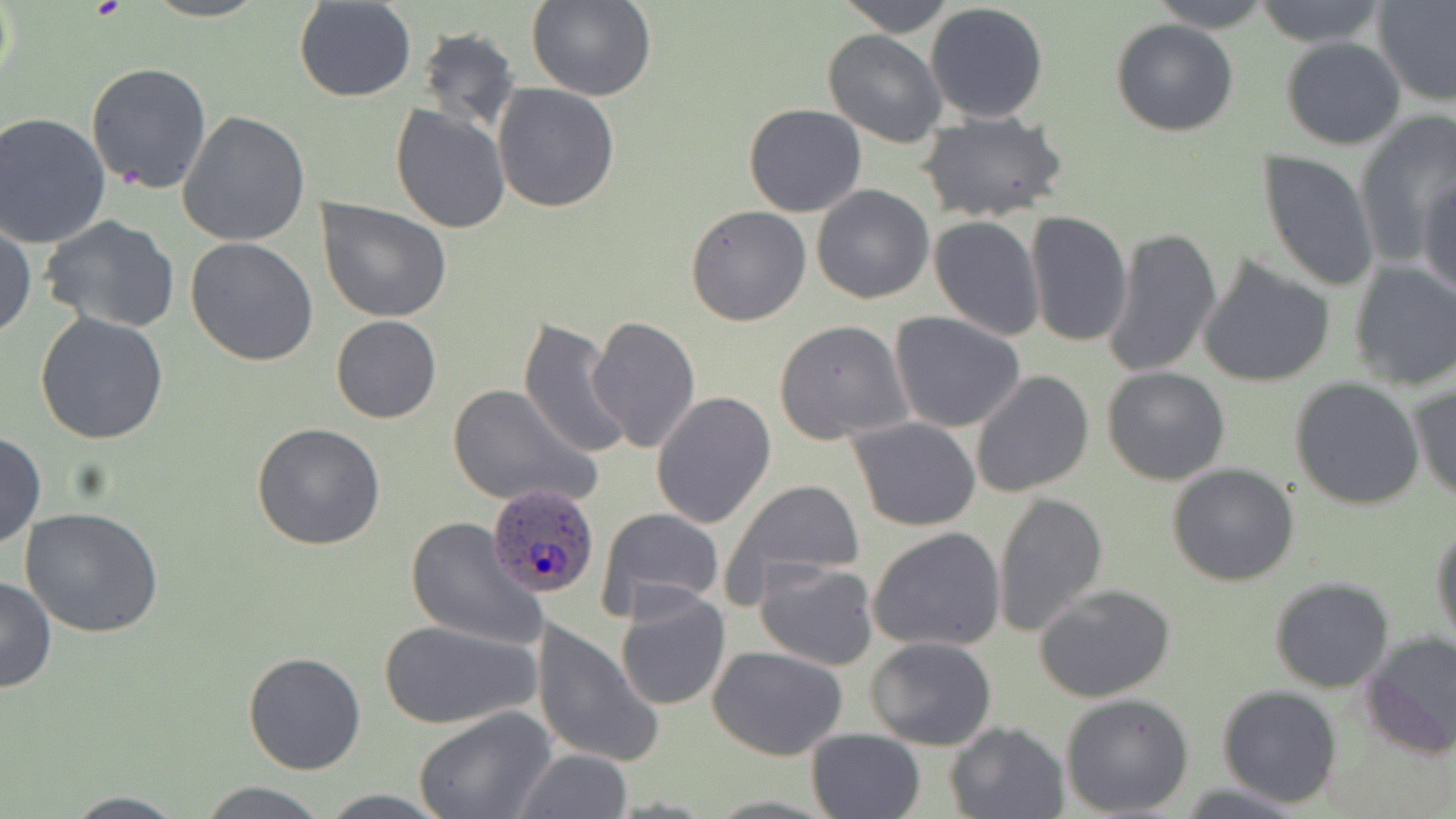 Approximate bounding boxes as [x1, y1, x2, y2] in pixels. Platelet locations: [88, 0, 129, 23]. Plasmodium ovale-infected red blood cell locations: [478, 486, 597, 604]. Uninfected red blood cell locations: [836, 0, 956, 36], [1148, 0, 1277, 32], [1251, 0, 1389, 48], [293, 1, 417, 102], [526, 1, 658, 103], [1373, 1, 1456, 105], [925, 3, 1050, 124], [1110, 18, 1239, 136], [415, 28, 522, 133], [822, 29, 947, 147], [1280, 37, 1406, 151], [85, 62, 212, 195], [492, 83, 620, 213], [743, 103, 867, 217], [389, 105, 510, 232], [178, 111, 311, 247], [919, 112, 1068, 224], [1353, 112, 1456, 265], [1, 113, 114, 250], [760, 115, 904, 263], [1258, 150, 1379, 292], [1420, 173, 1456, 301], [811, 184, 935, 304], [318, 198, 451, 323], [685, 204, 811, 325], [1024, 211, 1131, 348], [930, 215, 1045, 340], [40, 216, 182, 334], [0, 220, 36, 341], [1101, 223, 1224, 381], [186, 238, 318, 367], [1198, 256, 1336, 388], [1347, 261, 1456, 392], [889, 311, 1026, 432], [34, 312, 169, 445], [330, 315, 441, 424], [587, 316, 701, 454], [516, 320, 630, 460], [773, 320, 915, 444], [1101, 366, 1231, 485], [970, 369, 1094, 498], [1291, 377, 1425, 509], [1408, 380, 1456, 504], [447, 382, 598, 509], [651, 392, 776, 529], [847, 417, 982, 532], [252, 423, 385, 551], [0, 431, 45, 549], [1167, 463, 1300, 587], [721, 478, 866, 600], [992, 491, 1107, 639], [19, 506, 164, 638], [594, 507, 727, 623], [405, 516, 544, 651], [1431, 518, 1455, 654], [866, 526, 1007, 653], [753, 558, 878, 672], [0, 576, 57, 693], [1268, 577, 1395, 693], [1034, 583, 1176, 702], [614, 588, 732, 710], [377, 618, 541, 731], [529, 619, 662, 769], [1361, 630, 1456, 758], [866, 636, 998, 750], [708, 645, 848, 759], [243, 650, 366, 775], [1216, 685, 1343, 808], [1059, 693, 1195, 817], [414, 708, 559, 819], [944, 721, 1069, 818], [805, 728, 926, 818], [513, 749, 631, 818], [195, 780, 334, 818], [314, 789, 455, 819], [61, 792, 191, 819]. Slide-level diagnosis: Plasmodium ovale. One field of a larger specimen. 1000x magnification. May-Grünwald-Giemsa stain. Thin blood smear. Optical microscopy. Image is 1456×819 pixels.